Report the malaria status of this cell.
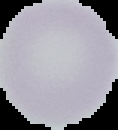

It is uninfected.

The area outside the segmented cell region is set to black. From a thin blood film. Image is 118×130 pixels.